Identify the parasite.
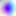
Toxoplasma gondii.

Captured at 400x magnification. Photomicrograph.